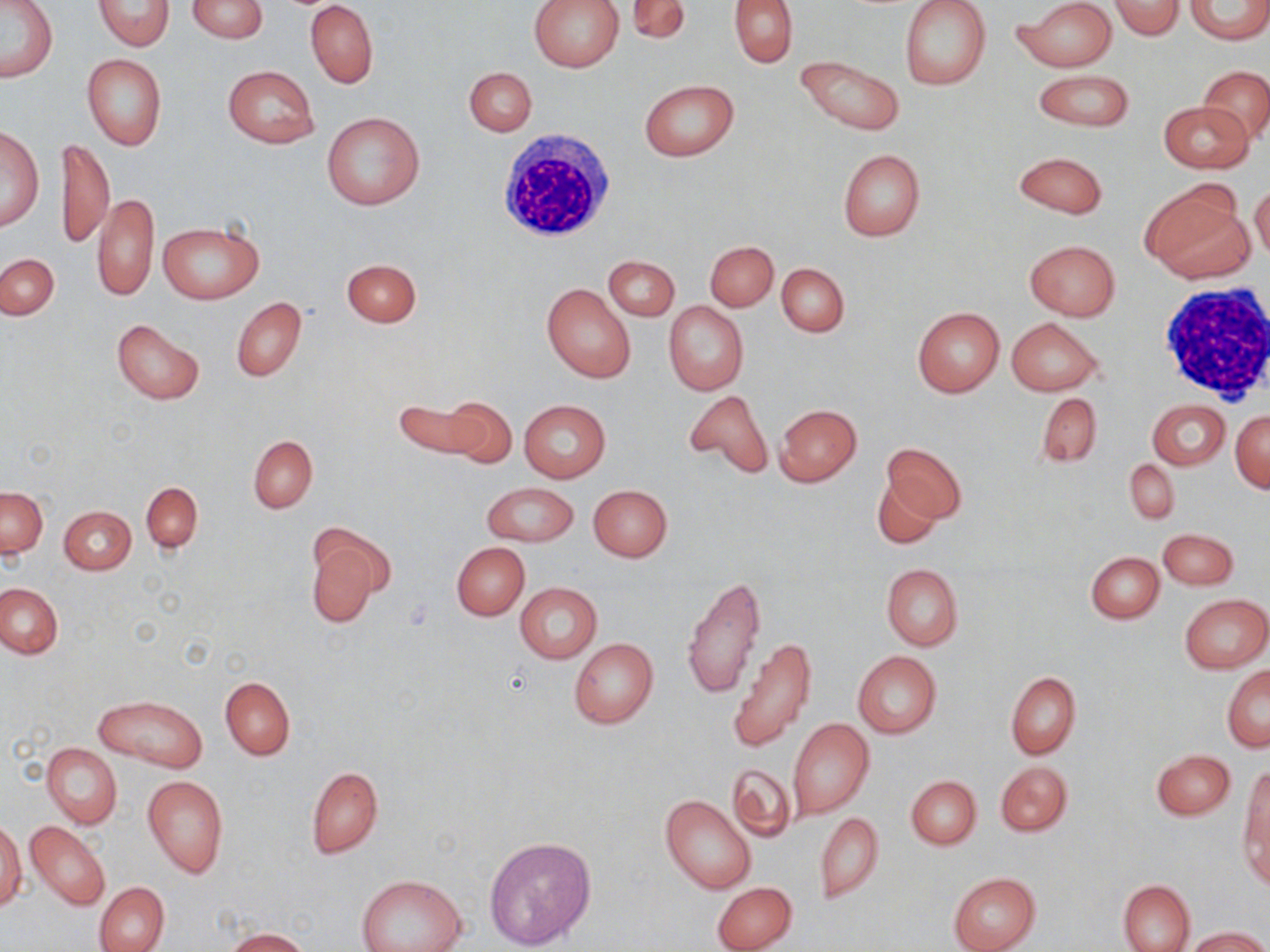
Summary:
  - Coordinate format: approximate bounding boxes as (x1, y1, x2, y2) in pixels
  - White blood cell locations: (496, 131, 616, 243), (1157, 281, 1270, 404)
  - Uninfected red blood cell locations: (93, 0, 175, 50), (187, 0, 267, 42), (625, 0, 690, 45), (729, 0, 797, 68), (1016, 0, 1117, 71), (1109, 0, 1184, 40), (1184, 0, 1270, 43), (1, 1, 59, 82), (305, 1, 378, 87), (530, 1, 623, 73), (899, 1, 992, 90), (82, 53, 167, 151), (794, 54, 905, 135), (1198, 64, 1270, 144), (222, 65, 319, 148), (464, 66, 537, 135), (1031, 70, 1136, 132), (639, 79, 740, 162), (1159, 101, 1253, 173), (323, 111, 425, 212), (0, 127, 43, 231), (58, 137, 114, 248), (837, 149, 925, 241), (1013, 151, 1108, 218), (1141, 181, 1252, 283), (1249, 185, 1269, 264), (93, 191, 160, 303), (158, 221, 264, 303), (1024, 239, 1121, 321), (705, 241, 778, 311), (1, 253, 58, 320), (605, 255, 679, 321), (342, 258, 421, 327), (776, 262, 849, 337), (542, 283, 636, 384), (232, 297, 306, 381), (663, 301, 748, 396), (912, 306, 1004, 397), (1006, 316, 1103, 396), (112, 318, 205, 405), (682, 388, 773, 481), (1035, 392, 1103, 467), (439, 396, 519, 468), (393, 399, 491, 460), (519, 399, 612, 482), (1147, 399, 1230, 470), (776, 405, 862, 487), (1230, 409, 1269, 493), (249, 436, 317, 512), (880, 441, 966, 525), (1126, 458, 1179, 524), (872, 476, 942, 550), (142, 482, 202, 553), (482, 482, 579, 546), (588, 484, 672, 562), (1, 485, 48, 557), (60, 505, 136, 574), (303, 524, 392, 630), (1157, 528, 1239, 589), (452, 543, 529, 620), (1086, 551, 1164, 624), (881, 563, 963, 652), (682, 574, 766, 701), (0, 583, 62, 660), (516, 584, 602, 662), (1180, 594, 1270, 673), (728, 637, 818, 753), (568, 638, 659, 729), (852, 650, 941, 739), (1223, 665, 1269, 751), (1005, 671, 1081, 760), (220, 676, 295, 759), (96, 695, 207, 770), (787, 717, 874, 819), (43, 743, 122, 828), (1150, 748, 1235, 819), (995, 761, 1073, 836), (726, 762, 799, 844), (306, 766, 383, 859), (1240, 767, 1269, 882), (142, 776, 229, 878), (906, 776, 980, 849), (660, 795, 756, 894), (815, 813, 882, 901), (24, 819, 111, 911), (1, 821, 25, 912), (484, 836, 596, 952), (948, 871, 1040, 952), (356, 874, 465, 952), (1118, 879, 1195, 952), (712, 881, 797, 952), (95, 882, 168, 952), (1186, 927, 1267, 952), (221, 928, 312, 951)
  - Slide-level diagnosis: negative for blood parasites
  - Magnification: 1000x
  - Image size: 1270×952 pixels
  - Preparation: thin blood smear
  - Modality: optical microscopy
  - Field of view: one of a larger specimen
  - Stain: May-Grünwald-Giemsa